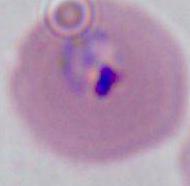

Summary:
  - Modality: photomicrograph
  - Magnification: 400x or 1000x
  - Identification: Plasmodium